Report the malaria status of this cell.
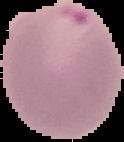

Parasitized.

Summary:
  - Image size: 124×142 pixels
  - Preparation: thin blood film
  - Image type: segmented cell region on a black background